Assess the morphology of the erythrocytes.
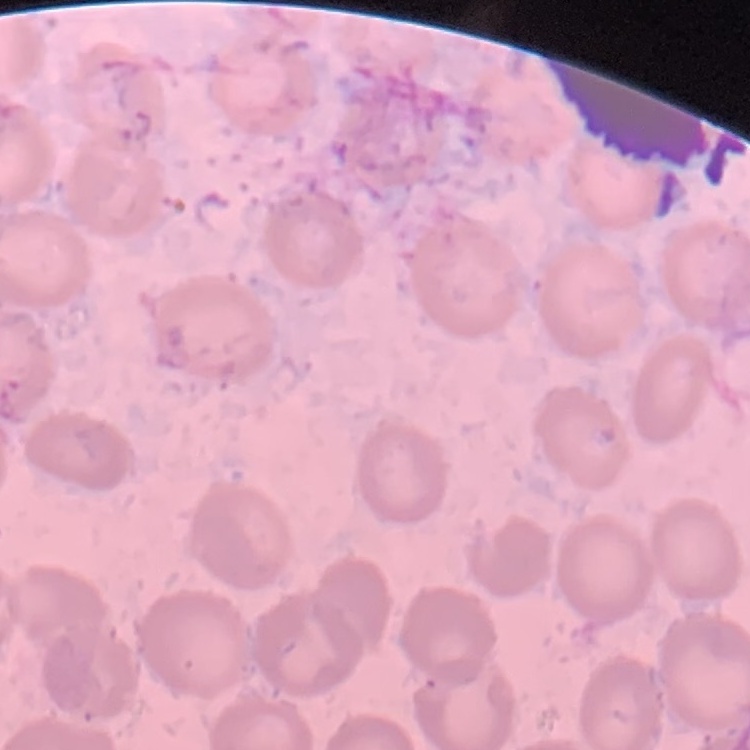
They show no rouleaux formation.

Summary:
  - Stain: Field's or Giemsa
  - Image type: one tile cut from a larger photomicrograph
  - Preparation: thin blood film